Identify the parasite.
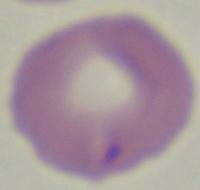

This is Babesia.

Micrograph. 1000x magnification.